Report the malaria status of this cell.
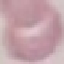

It is uninfected.

Summary:
  - Capture: smartphone through the microscope eyepiece
  - Image type: automatically extracted cell patch, resized to 64 × 64 pixels
  - Stain: Giemsa
  - Preparation: thin blood film